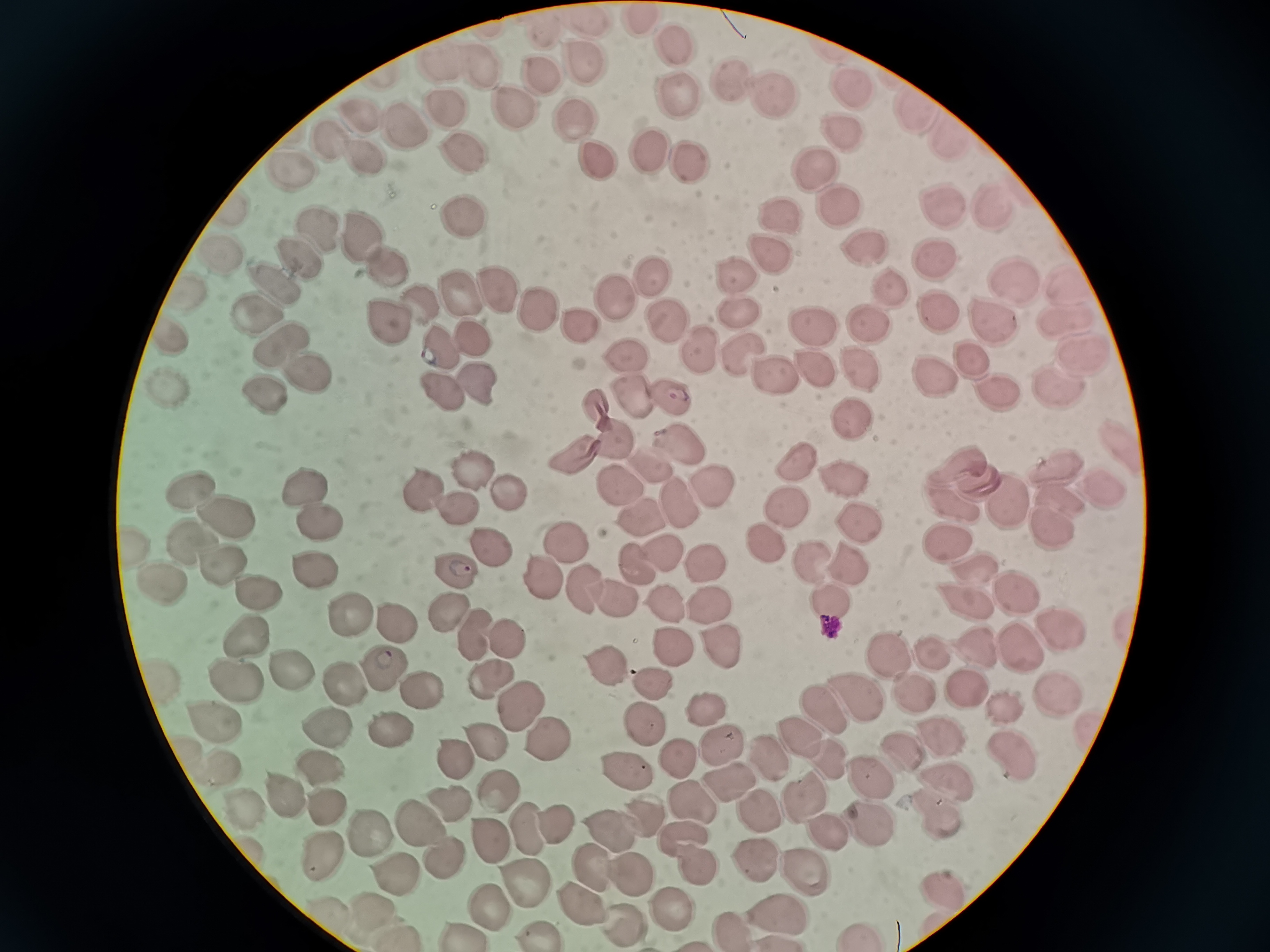
cell locations = approximate centers as (x, y) in pixels: (638, 22), (585, 25), (537, 31), (664, 41), (574, 60), (437, 63), (478, 68), (536, 79), (731, 80), (849, 81), (758, 98), (681, 102), (447, 106), (510, 109), (917, 110), (356, 114), (574, 122), (396, 128), (850, 134), (944, 134), (324, 139), (646, 149), (355, 154), (465, 159), (683, 161), (812, 163), (285, 166), (597, 166), (834, 195), (228, 206), (939, 206), (991, 207), (459, 218), (773, 218), (326, 238), (362, 238), (862, 252), (213, 253), (767, 255), (941, 257), (296, 258), (393, 272), (998, 276), (739, 280), (888, 284), (495, 286), (277, 287), (658, 287), (1068, 289), (180, 290), (464, 291), (614, 299), (548, 307), (933, 308), (425, 309), (734, 310), (997, 314), (265, 316), (865, 318), (1067, 318), (582, 320), (394, 324), (667, 326), (163, 333), (469, 334), (813, 335), (281, 341), (439, 347), (701, 348), (1083, 348), (743, 354), (630, 358), (974, 362), (810, 367), (859, 367), (775, 372), (311, 379), (477, 379), (167, 382), (930, 382), (1065, 382), (996, 388), (437, 391), (627, 391), (266, 397), (669, 397), (595, 410), (852, 419), (613, 442), (680, 447), (567, 456), (1119, 457), (796, 461), (1049, 465), (954, 467), (479, 470), (649, 470), (837, 471), (975, 483), (613, 484), (423, 488), (192, 489), (1093, 490), (308, 491), (510, 494), (715, 494), (1054, 495), (675, 500), (1003, 501), (949, 502), (781, 505), (462, 506), (640, 509), (226, 517), (320, 522), (860, 522), (1044, 523), (944, 537), (771, 538), (134, 543), (567, 543), (487, 545), (659, 545), (632, 556), (810, 556), (705, 561), (317, 564), (846, 564), (224, 565), (457, 566), (974, 568), (549, 572), (165, 582), (252, 586), (587, 590), (1010, 590), (620, 595), (668, 601), (829, 601), (447, 603), (966, 603), (710, 610), (354, 615), (398, 617), (1053, 627), (479, 634), (507, 634), (244, 638), (666, 640), (720, 641), (1024, 643), (973, 651), (931, 653), (886, 654), (607, 660), (386, 666), (289, 673), (159, 675), (237, 675), (483, 676), (655, 682), (345, 684), (906, 684), (422, 688), (959, 692), (1057, 692), (850, 693), (998, 702), (520, 707), (821, 707), (708, 710), (211, 712), (646, 722), (327, 727), (390, 730), (937, 735), (799, 736), (720, 737), (551, 739), (486, 743), (1013, 750), (897, 751), (827, 753), (460, 756), (682, 756), (774, 763), (320, 765), (222, 768), (619, 771), (943, 780), (732, 786), (868, 786), (494, 790), (277, 791), (804, 798), (446, 805), (934, 806), (238, 807), (320, 807), (640, 811), (764, 814), (415, 820), (863, 821), (521, 824), (546, 824), (610, 830), (364, 831), (825, 832), (489, 836), (312, 852), (441, 856), (755, 859), (591, 864), (630, 867), (796, 869), (394, 876), (525, 880), (939, 890), (486, 903), (581, 903), (671, 908), (373, 911), (772, 913), (621, 921), (536, 932), (459, 933)
field of view = single
image size = 1270×952 pixels
preparation = thin smear
capture = smartphone camera at the microscope eyepiece
stain = Giemsa